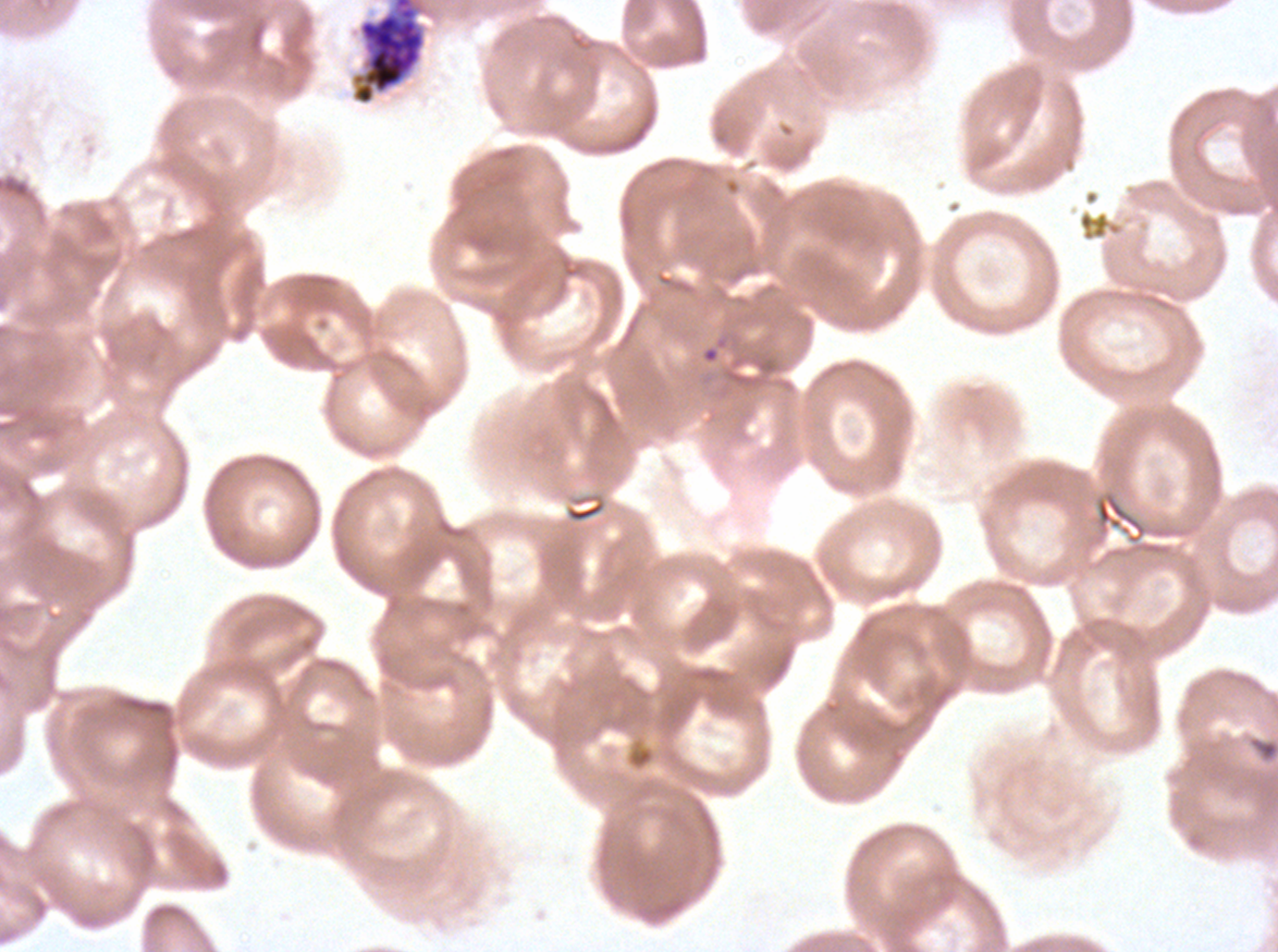 Approximate bounding boxes as {x1, y1, x2, y2} in pixels. Late schizont locations: {351, 0, 426, 105}. Giemsa-stained preparation. Thin blood smear. One sub-image of a larger composite. Image is 1278×952 pixels. P. falciparum cultured ex vivo for 24 to 48 hours, from a patient in The Gambia.